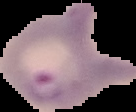

malaria status = parasitized
image size = 136×112 pixels
preparation = thin blood film
image type = cell region segmented out of the field of view; surrounding area masked to black